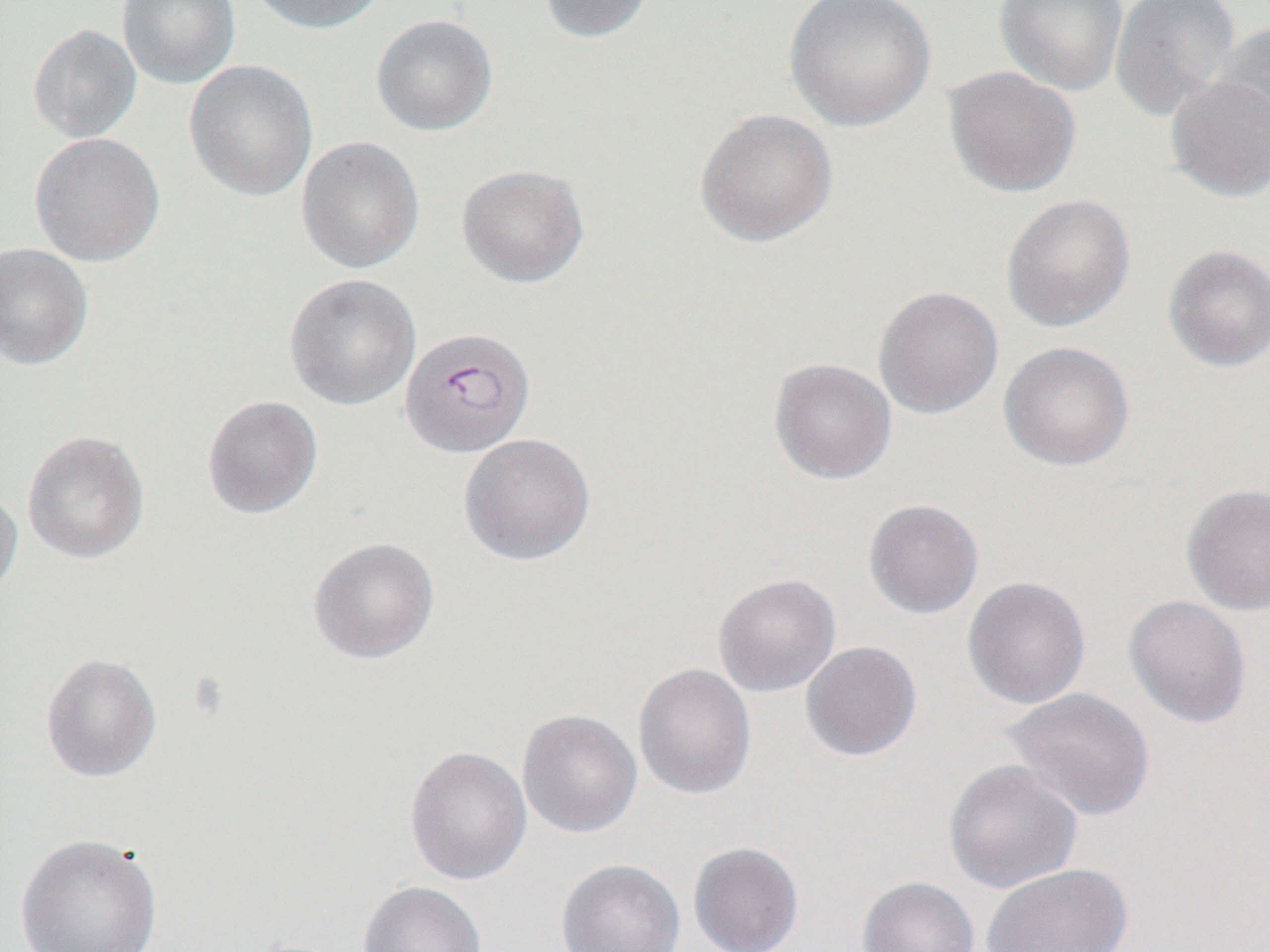

{
  "slide_level_diagnosis": "Plasmodium falciparum",
  "field_of_view": "single",
  "preparation": "thin blood smear",
  "modality": "optical microscopy",
  "plasmodium_falciparum_infected_red_blood_cell_locations": "approximate bounding boxes as (x1, y1, x2, y2) in pixels: (398, 327, 535, 458)",
  "magnification": "1000x",
  "image_size": "1270×952 pixels",
  "uninfected_red_blood_cell_locations": "approximate bounding boxes as (x1, y1, x2, y2) in pixels: (117, 0, 241, 89), (247, 0, 388, 35), (537, 0, 657, 43), (783, 0, 937, 132), (993, 0, 1129, 96), (1109, 0, 1242, 123), (371, 14, 497, 136), (1212, 19, 1270, 154), (27, 23, 142, 143), (184, 59, 318, 201), (943, 66, 1082, 197), (1165, 73, 1270, 203), (695, 108, 838, 248), (28, 132, 165, 267), (297, 136, 424, 274), (456, 164, 589, 288), (1001, 194, 1136, 332), (0, 242, 93, 369), (1163, 243, 1270, 372), (284, 274, 421, 411), (873, 286, 1004, 419), (999, 341, 1134, 472), (769, 358, 897, 485), (202, 395, 323, 519), (21, 430, 150, 564), (458, 433, 596, 566), (1181, 483, 1270, 616), (0, 485, 23, 606), (863, 499, 984, 619), (308, 536, 440, 664), (713, 574, 841, 697), (962, 576, 1090, 709), (1124, 595, 1252, 729), (800, 641, 922, 761), (40, 653, 162, 782), (633, 663, 756, 800), (1003, 687, 1156, 822), (517, 709, 642, 838), (404, 745, 531, 885), (943, 759, 1084, 895), (16, 833, 163, 952), (688, 842, 804, 952), (556, 859, 685, 952), (981, 862, 1133, 952), (856, 876, 980, 952), (358, 881, 487, 952)"
}